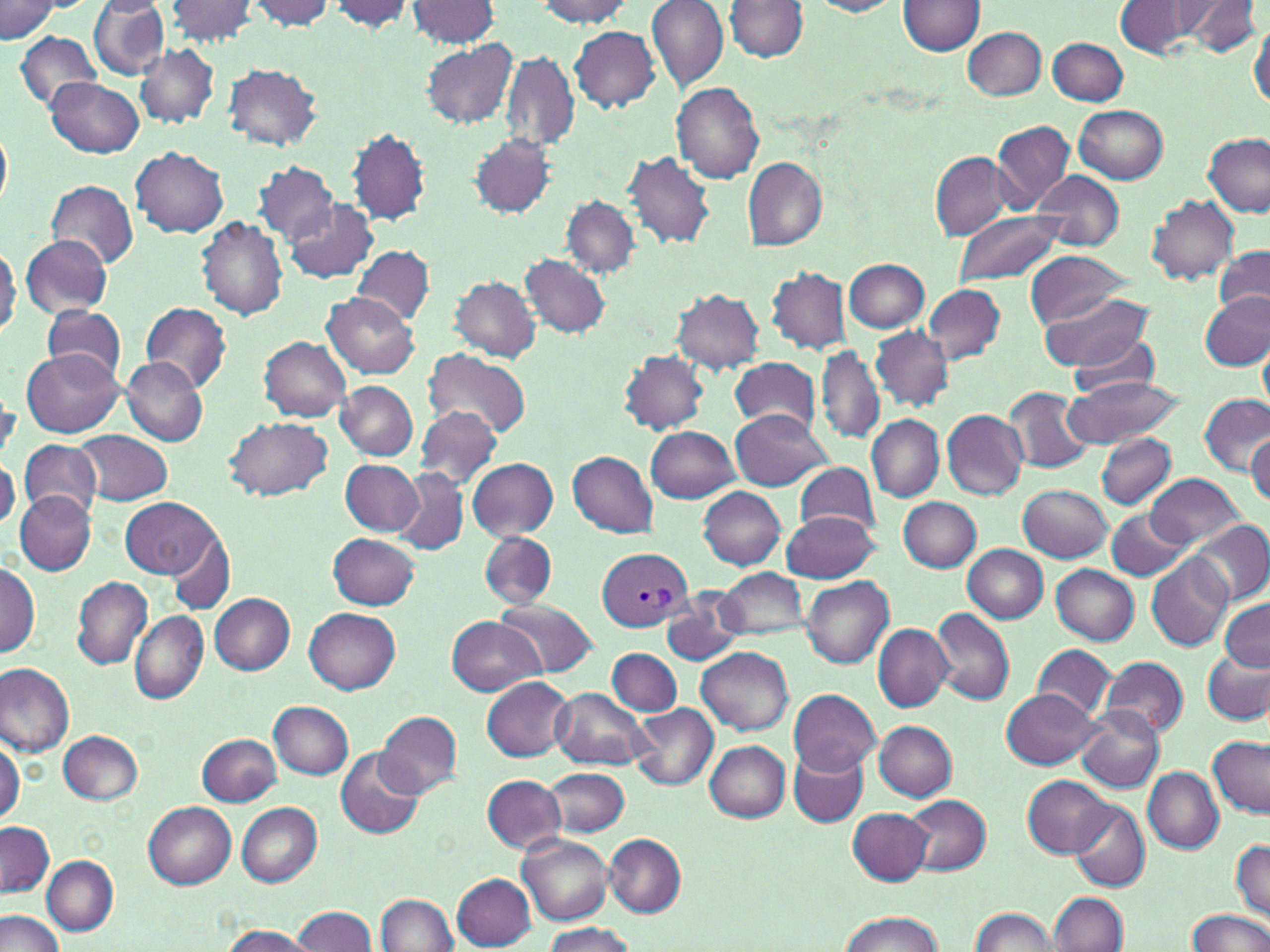
Approximate bounding boxes as (x1,y1)-(x2,y2) corner pairs in pixels. Uninfected red blood cell locations: (87,0)-(171,80), (166,0)-(259,46), (325,0)-(414,33), (407,0)-(501,47), (535,0)-(638,27), (647,0)-(729,93), (899,0)-(986,56), (1171,0)-(1260,52), (0,1)-(58,45), (247,1)-(338,31), (804,1)-(905,17), (725,2)-(807,63), (1114,2)-(1204,58), (1249,19)-(1270,115), (570,25)-(660,113), (963,27)-(1046,101), (14,30)-(100,110), (1046,36)-(1128,106), (420,39)-(517,129), (135,44)-(219,127), (501,51)-(580,151), (223,62)-(323,150), (45,77)-(144,157), (673,83)-(765,183), (1074,105)-(1168,182), (990,119)-(1074,213), (0,124)-(12,213), (346,128)-(431,226), (1201,132)-(1270,217), (469,133)-(556,218), (131,147)-(228,237), (624,151)-(715,249), (930,152)-(1012,239), (741,157)-(826,250), (253,161)-(338,244), (1034,169)-(1124,252), (45,181)-(138,267), (563,195)-(640,279), (1147,195)-(1240,284), (282,197)-(379,282), (953,212)-(1062,288), (197,216)-(288,320), (21,233)-(112,319), (0,243)-(19,338), (351,245)-(435,325), (1214,247)-(1270,319), (1024,251)-(1134,329), (521,254)-(611,338), (843,259)-(929,331), (767,266)-(850,353), (450,276)-(541,361), (923,282)-(1006,364), (672,289)-(765,372), (1041,290)-(1154,373), (1200,291)-(1270,370), (323,293)-(420,379), (140,302)-(232,394), (43,304)-(126,386), (871,325)-(952,410), (1067,333)-(1163,400), (259,337)-(352,422), (1259,339)-(1269,415), (817,344)-(883,444), (22,348)-(125,437), (422,349)-(531,440), (619,351)-(709,434), (122,357)-(208,447), (729,357)-(821,432), (1064,377)-(1183,448), (337,381)-(418,460), (1007,387)-(1094,474), (1197,393)-(1270,473), (414,406)-(504,491), (729,409)-(831,491), (941,410)-(1029,499), (225,415)-(335,498), (868,415)-(943,500), (646,426)-(738,503), (73,430)-(173,505), (1096,432)-(1176,510), (1247,434)-(1270,505), (19,440)-(102,521), (568,451)-(657,537), (469,458)-(558,541), (341,460)-(426,536), (793,461)-(881,540), (0,463)-(19,542), (395,470)-(468,557), (1147,473)-(1246,547), (1018,485)-(1111,562), (698,486)-(785,570), (15,492)-(96,575), (122,497)-(219,577), (899,497)-(981,572), (1105,508)-(1190,580), (782,511)-(879,582), (1193,519)-(1269,603), (167,529)-(235,613), (480,531)-(557,610), (328,533)-(418,609), (962,543)-(1047,623), (1147,553)-(1233,652), (1,562)-(38,656), (1051,565)-(1138,644), (718,568)-(809,640), (800,576)-(893,668), (72,577)-(152,670), (664,590)-(748,667), (209,593)-(295,673), (1219,598)-(1270,669), (493,599)-(599,677), (930,606)-(1016,707), (305,607)-(401,692), (130,611)-(208,705), (447,616)-(545,696), (872,624)-(954,712), (1034,645)-(1115,718), (695,646)-(793,735), (606,647)-(682,716), (1204,649)-(1270,724), (1100,656)-(1189,737), (0,663)-(75,757), (482,676)-(573,761), (1000,687)-(1103,768), (551,688)-(651,769), (789,689)-(880,775), (269,700)-(353,780), (630,703)-(719,791), (1078,707)-(1165,794), (375,710)-(463,799), (874,721)-(957,800), (58,729)-(142,804), (198,733)-(283,806), (1208,736)-(1270,816), (705,741)-(790,822), (0,742)-(22,824), (790,748)-(870,827), (335,751)-(423,838), (546,767)-(628,836), (1142,767)-(1223,853), (482,775)-(566,853), (1024,775)-(1113,857), (905,794)-(990,876), (1068,800)-(1150,893), (142,801)-(235,888), (236,802)-(321,886), (849,809)-(933,885), (0,823)-(54,898), (518,834)-(612,924), (604,834)-(685,918), (1231,839)-(1270,920), (42,856)-(118,936), (453,874)-(537,950), (1049,892)-(1128,952), (376,894)-(459,952), (291,906)-(377,952), (970,908)-(1058,951), (1184,909)-(1270,952), (0,910)-(65,952), (838,912)-(944,951), (541,921)-(635,952), (219,923)-(317,952). Plasmodium vivax-infected red blood cell locations: (596,547)-(695,632). Slide-level diagnosis: Plasmodium vivax. May-Grünwald-Giemsa stain. Image is 1270×952 pixels. Light microscopy. 1000x magnification. Thin blood smear. Single field of view.